Name the parasite shown.
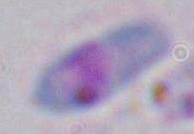

This is Toxoplasma gondii.

modality = micrograph
magnification = 1000x